Locate every Plasmodium parasite.
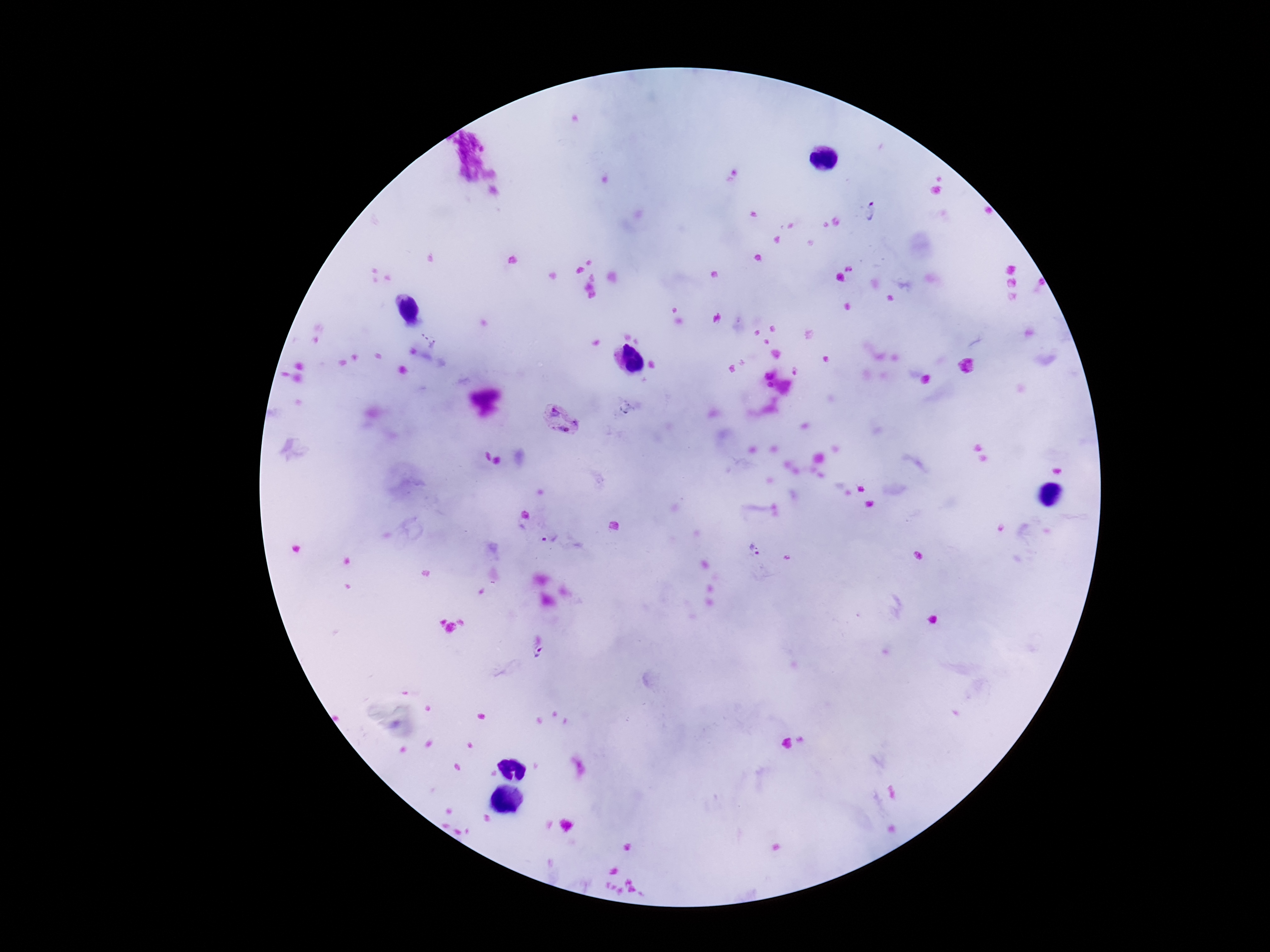
Approximate centers as {x, y} in pixels.
Plasmodium parasites: {873, 213}, {560, 420}, {526, 514}, {553, 539}, {755, 550}, {540, 649}.

field_of_view: single
patient_malaria_status: infected
image_size: 1270×952 pixels
stain: Giemsa
capture: smartphone camera through the microscope eyepiece
magnification: 100x
preparation: thick blood film